Assess for malaria.
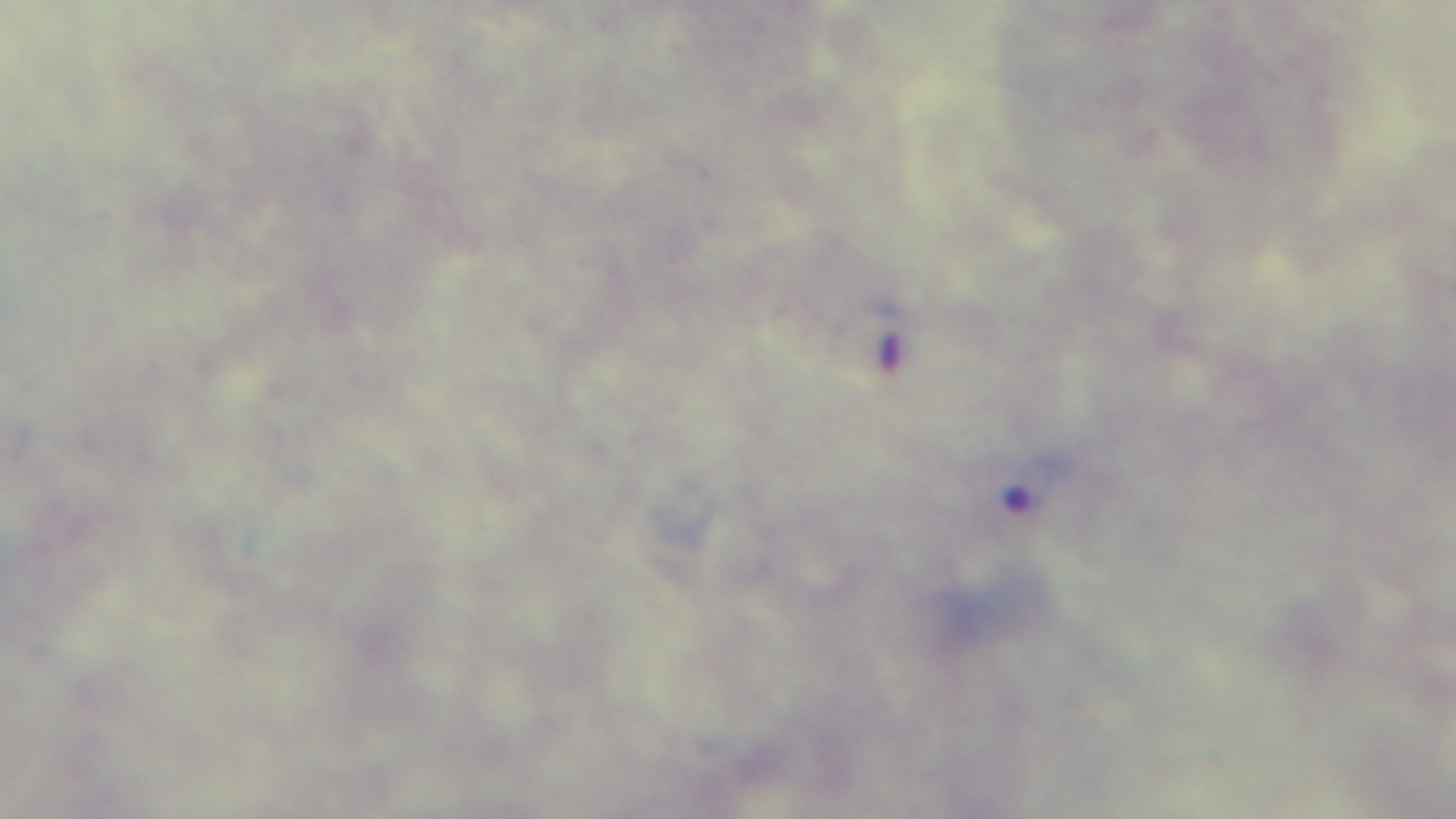

Infected.

Summary:
  - Stain: Giemsa
  - Capture: mounted 4K digital camera
  - Field of view: single
  - Preparation: thick blood film
  - Objective: 100x oil immersion
  - Modality: light microscopy